Report the malaria status of this cell.
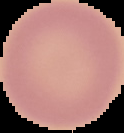

It is uninfected.

preparation = thin blood smear
image type = segmented cell region with the area outside set to black
image size = 124×133 pixels